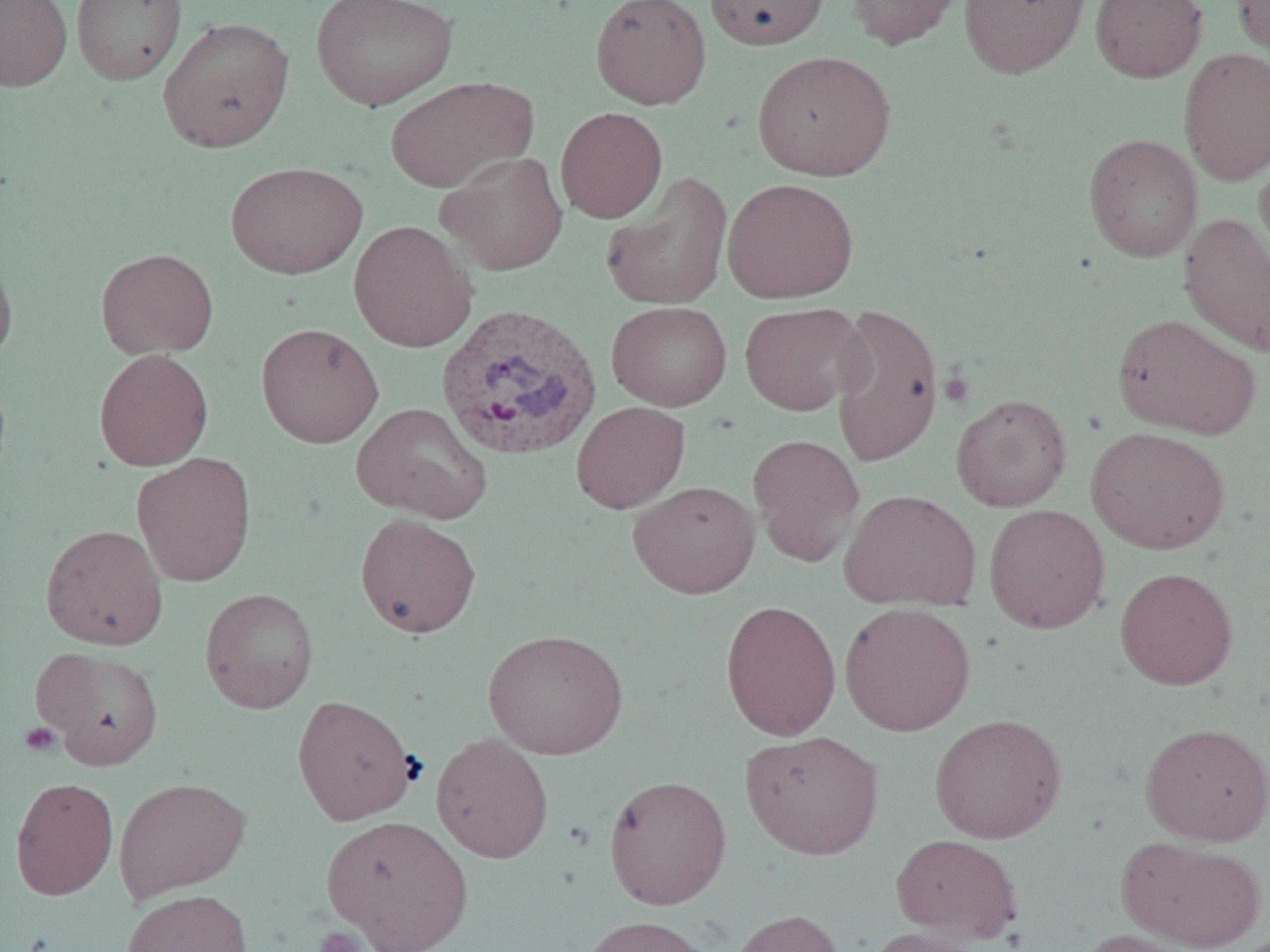
Summary:
  - Coordinate format: approximate bounding boxes as (x1,y1)-(x2,y2) corner pairs in pixels
  - Platelet locations: (939,371)-(973,407), (18,722)-(61,758), (312,927)-(369,952)
  - Uninfected red blood cell locations: (0,0)-(72,92), (71,0)-(187,85), (311,0)-(458,111), (590,0)-(712,109), (704,0)-(830,50), (845,0)-(964,51), (959,0)-(1090,79), (1089,0)-(1207,83), (1232,0)-(1270,63), (157,16)-(294,152), (1178,47)-(1270,185), (752,50)-(895,181), (384,76)-(537,192), (555,107)-(668,223), (1083,133)-(1203,262), (435,151)-(568,275), (1254,151)-(1270,278), (226,161)-(368,279), (601,171)-(733,311), (722,178)-(859,303), (1178,213)-(1270,356), (348,221)-(478,352), (0,248)-(18,365), (96,248)-(218,359), (607,301)-(732,411), (739,302)-(867,416), (829,302)-(944,468), (1112,313)-(1261,439), (256,322)-(384,448), (93,349)-(213,471), (951,393)-(1072,512), (571,401)-(690,513), (352,402)-(493,524), (1086,426)-(1230,555), (747,433)-(865,567), (132,453)-(257,588), (627,480)-(760,599), (839,489)-(981,612), (984,504)-(1110,634), (354,512)-(481,638), (41,524)-(168,650), (1115,567)-(1238,690), (199,588)-(319,714), (720,600)-(841,740), (839,602)-(976,736), (483,628)-(628,760), (33,646)-(164,770), (292,694)-(418,825), (929,713)-(1067,844), (1139,722)-(1270,846), (740,730)-(884,860), (431,732)-(553,864), (603,775)-(732,910), (10,777)-(118,900), (113,777)-(251,902), (320,815)-(474,952), (891,833)-(1022,944), (1118,837)-(1266,951), (121,889)-(253,952), (728,909)-(846,952), (579,915)-(716,952), (863,926)-(991,952), (1079,928)-(1204,952)
  - Plasmodium vivax-infected red blood cell locations: (434,303)-(603,461)
  - Slide-level diagnosis: Plasmodium vivax
  - Field of view: one of a larger specimen
  - Modality: light microscopy
  - Preparation: thin blood film
  - Image size: 1270×952 pixels
  - Magnification: 1000x